Look for parasitized red blood cells.
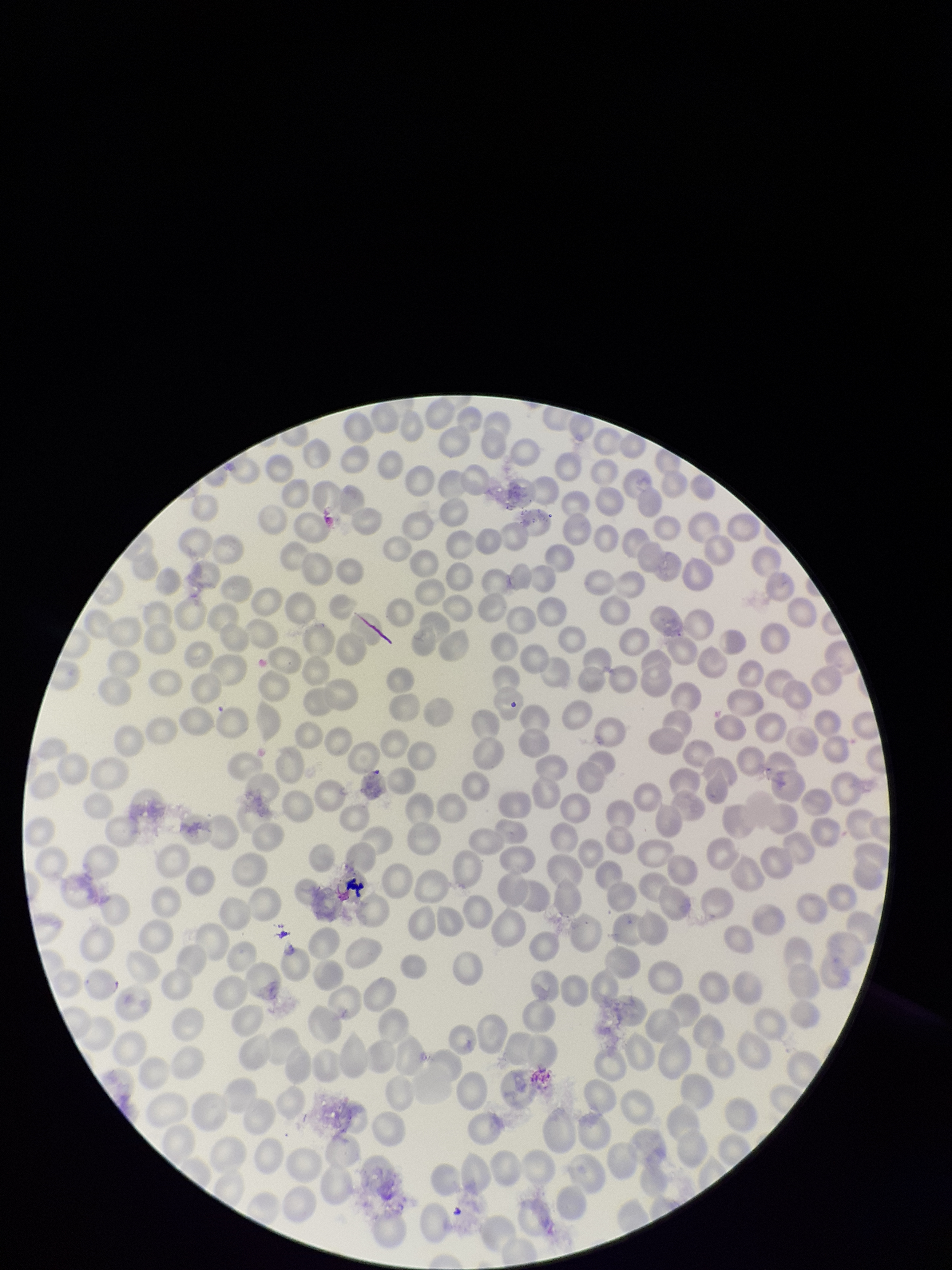
None detected.

image size = 952×1270 pixels
capture = smartphone photograph through the microscope eyepiece
field of view = single
species reported for this patient = Plasmodium falciparum
preparation = thin smear
parasitized red blood cell count = 0
red blood cell count = 286
patient malaria status = infected
stain = Giemsa